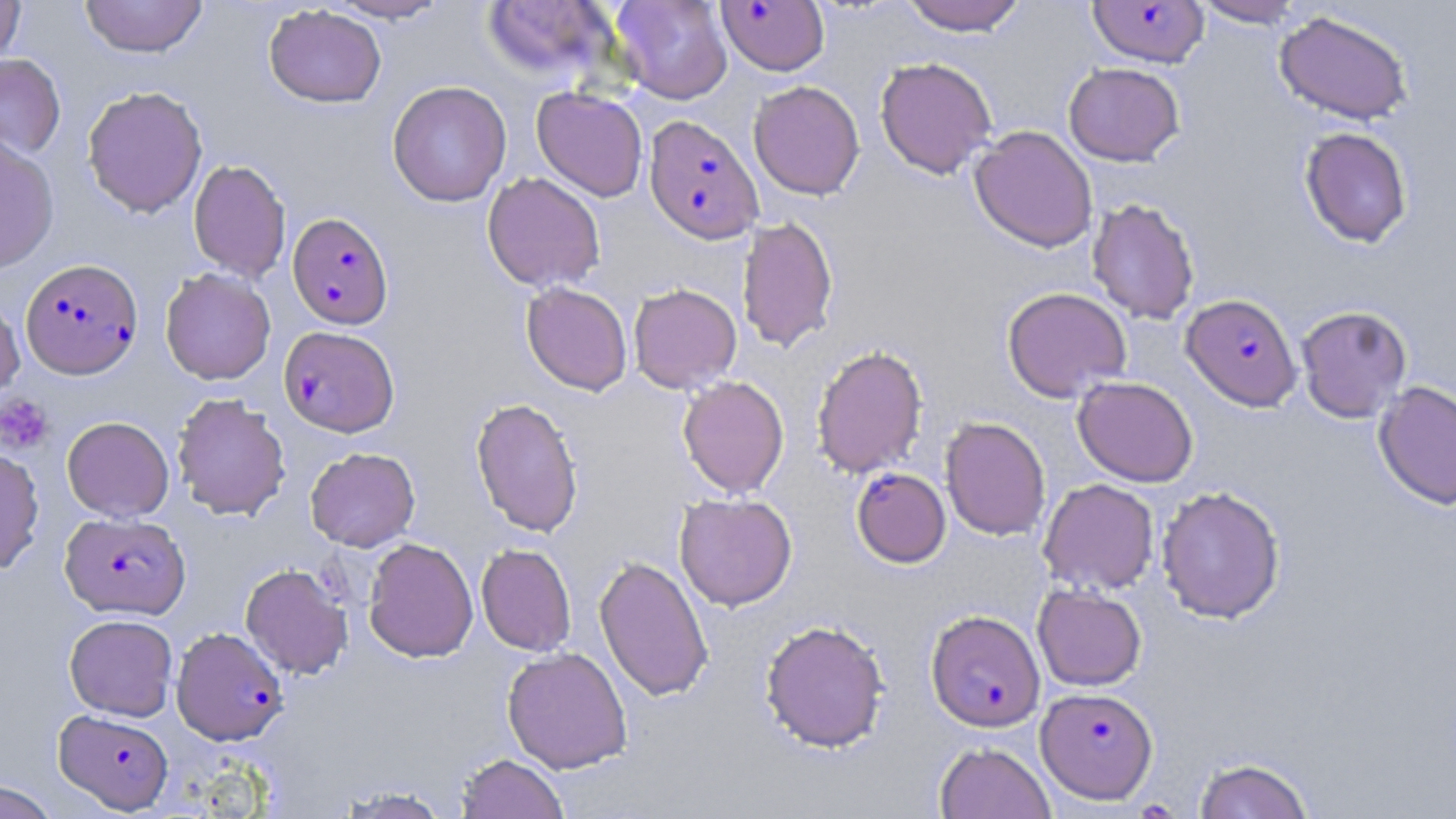
Summary:
  - Coordinate format: approximate bounding boxes as [x1, y1, x2, y2] in pixels
  - Uninfected red blood cell locations: [0, 0, 26, 64], [80, 0, 207, 58], [326, 0, 452, 23], [612, 0, 733, 104], [900, 0, 1028, 36], [1192, 0, 1308, 27], [481, 1, 619, 84], [264, 4, 386, 108], [1274, 10, 1414, 125], [0, 54, 66, 159], [874, 57, 997, 179], [1063, 62, 1185, 166], [387, 80, 511, 207], [748, 81, 865, 200], [82, 85, 208, 217], [532, 87, 648, 201], [969, 125, 1098, 253], [1299, 127, 1413, 248], [0, 134, 59, 274], [189, 159, 291, 282], [482, 172, 605, 292], [1086, 197, 1200, 325], [736, 215, 839, 354], [160, 268, 276, 385], [521, 282, 633, 396], [628, 283, 742, 393], [1002, 287, 1132, 402], [0, 293, 24, 404], [1296, 305, 1412, 422], [811, 344, 928, 479], [677, 375, 789, 498], [1072, 376, 1198, 487], [1374, 380, 1456, 510], [171, 392, 291, 520], [470, 397, 584, 537], [62, 416, 174, 521], [940, 416, 1051, 540], [305, 447, 420, 551], [0, 448, 44, 574], [1037, 478, 1160, 595], [1156, 486, 1285, 624], [674, 493, 797, 611], [364, 537, 478, 663], [476, 543, 576, 656], [594, 554, 713, 702], [240, 563, 353, 679], [1032, 585, 1147, 691], [64, 614, 178, 720], [760, 619, 890, 753], [502, 646, 633, 774], [934, 742, 1055, 819], [456, 753, 569, 819], [1193, 757, 1315, 819], [0, 779, 59, 819], [334, 786, 454, 818]
  - Platelet locations: [1, 393, 54, 455]
  - Plasmodium falciparum-infected red blood cell locations: [716, 1, 830, 76], [1087, 1, 1209, 68], [640, 115, 759, 244], [287, 211, 393, 329], [21, 258, 143, 379], [1182, 293, 1302, 411], [279, 326, 399, 436], [851, 466, 951, 568], [61, 512, 190, 619], [926, 609, 1045, 731], [172, 627, 288, 745], [1037, 687, 1158, 803], [54, 709, 174, 813]
  - Slide-level diagnosis: Plasmodium falciparum
  - Image size: 1456×819 pixels
  - Preparation: thin blood film
  - Magnification: 1000x
  - Stain: May-Grünwald-Giemsa
  - Field of view: single
  - Modality: light microscopy